State which cell type is depicted.
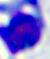

This is a leukocyte.

Summary:
  - Magnification: 400x
  - Modality: photomicrograph